Name the cell type shown.
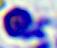
A leukocyte.

Summary:
  - Magnification: 400x
  - Modality: micrograph